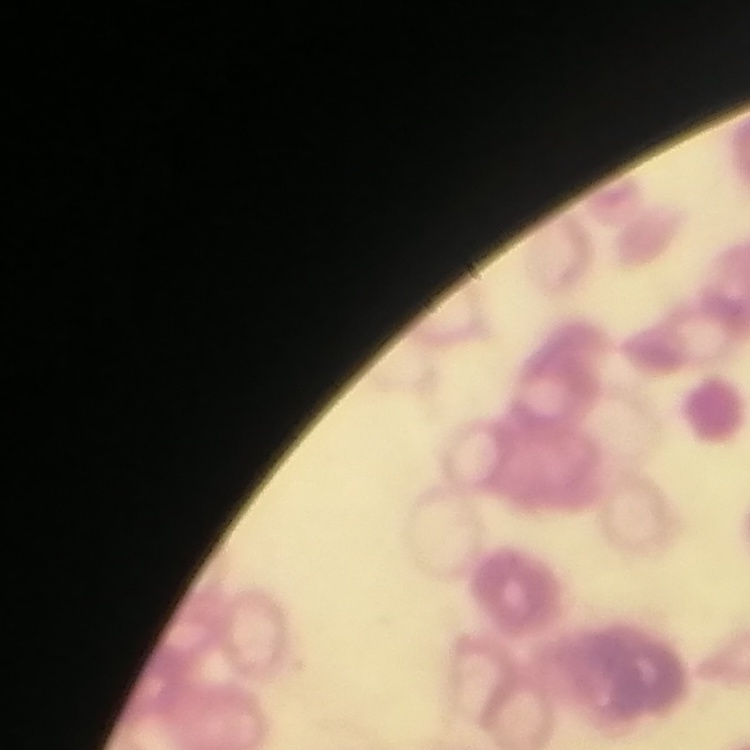 The red blood cells show rouleaux formation. One tile cut from a larger photomicrograph. Thin peripheral smear. Stained with either Field's or Giemsa.